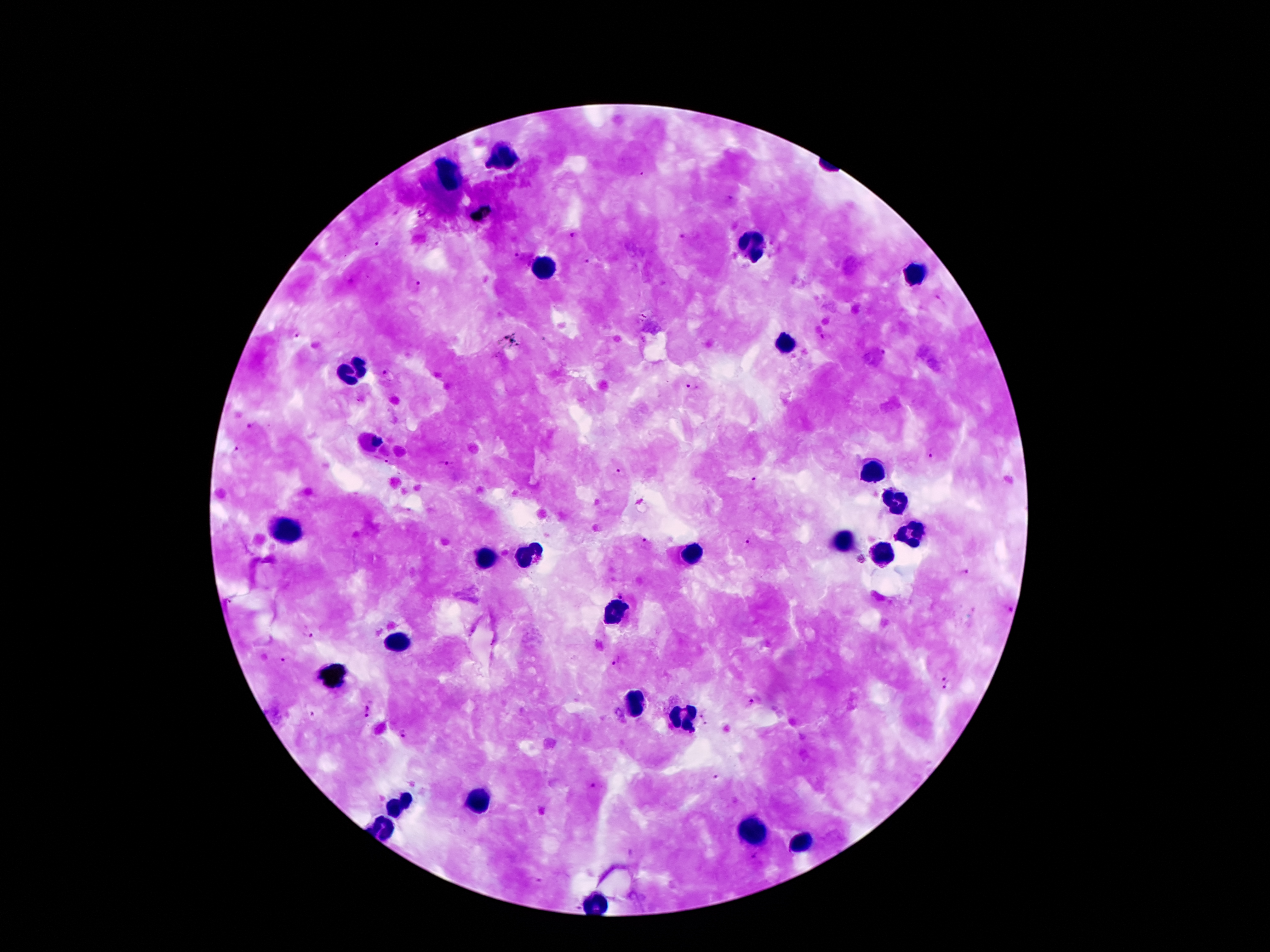 Approximate centers as {x, y} in pixels. Leukocyte locations: {506, 155}, {450, 178}, {754, 246}, {544, 268}, {914, 272}, {787, 344}, {354, 372}, {873, 470}, {894, 502}, {908, 527}, {290, 532}, {845, 540}, {692, 551}, {530, 555}, {888, 557}, {486, 560}, {616, 612}, {399, 642}, {634, 703}, {685, 718}, {479, 800}, {399, 803}, {384, 829}, {753, 833}, {804, 843}, {596, 906}. Malaria parasite locations: {728, 198}, {573, 235}, {682, 236}, {373, 242}, {517, 256}, {589, 260}, {415, 284}, {940, 300}, {296, 335}, {826, 336}, {385, 373}, {692, 388}, {251, 426}, {236, 451}, {933, 455}, {444, 463}, {387, 464}, {619, 473}, {755, 482}, {746, 543}, {645, 544}, {967, 573}, {622, 596}, {1008, 610}, {307, 634}, {282, 662}, {617, 662}, {941, 673}, {948, 688}, {753, 703}, {367, 710}, {702, 712}, {707, 725}, {403, 733}, {716, 777}, {594, 787}, {757, 857}, {536, 880}. Image is 1270×952 pixels. Photographed through the microscope eyepiece with a smartphone camera. Single field of view. Thick blood smear. Giemsa-stained preparation. 100x magnification. Patient malaria status: infected with Plasmodium falciparum.